Give the extent of all Plasmodium falciparum-infected red blood cells.
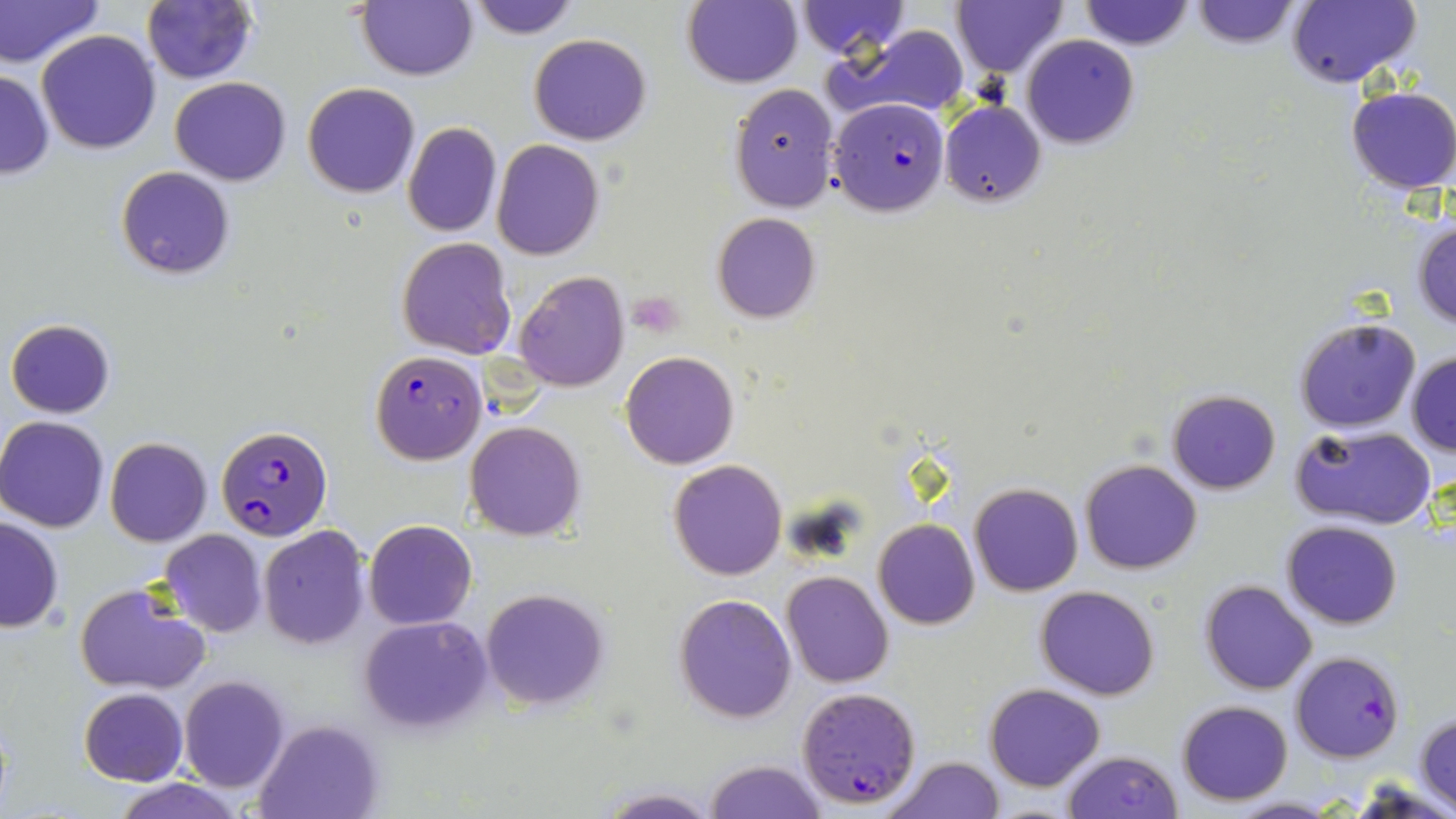
Approximate bounding boxes as (x1,y1)-(x2,y2) corner pairs in pixels.
Plasmodium falciparum-infected red blood cells: (829,97)-(950,216), (370,351)-(486,464), (217,424)-(332,541), (1291,650)-(1404,762), (797,686)-(923,810).

Summary:
  - Uninfected red blood cell locations: (0,0)-(104,69), (356,0)-(476,81), (465,0)-(579,39), (796,0)-(909,58), (951,0)-(1068,78), (1078,0)-(1196,52), (1289,0)-(1421,87), (140,1)-(258,85), (681,1)-(802,88), (1187,1)-(1303,51), (836,24)-(972,122), (37,31)-(161,154), (528,33)-(653,146), (1021,35)-(1139,148), (0,69)-(53,179), (169,77)-(292,185), (301,82)-(421,199), (729,83)-(840,213), (1345,86)-(1456,194), (939,101)-(1046,206), (401,122)-(501,237), (493,138)-(603,259), (115,165)-(235,279), (713,211)-(821,323), (1411,219)-(1456,330), (395,238)-(517,359), (513,272)-(629,392), (1294,317)-(1422,434), (5,318)-(115,418), (1406,350)-(1456,457), (621,351)-(739,469), (1166,388)-(1283,494), (0,416)-(111,532), (463,420)-(586,541), (1291,425)-(1439,531), (105,437)-(212,546), (669,457)-(788,580), (1080,459)-(1201,573), (969,483)-(1082,597), (0,516)-(65,633), (363,519)-(477,631), (874,519)-(980,630), (1281,520)-(1403,629), (257,526)-(370,649), (159,529)-(267,638), (780,570)-(893,686), (1200,580)-(1318,695), (74,581)-(211,695), (1036,585)-(1159,699), (480,588)-(609,711), (674,594)-(797,723), (359,617)-(493,735), (178,675)-(290,793), (984,682)-(1103,791), (78,689)-(186,786), (1176,700)-(1293,805), (1415,710)-(1456,813), (255,719)-(382,818), (1061,749)-(1183,818), (883,756)-(1004,819), (704,759)-(827,819), (111,777)-(243,819), (597,788)-(718,819), (1226,798)-(1343,819)
  - Platelet locations: (626,291)-(686,338)
  - Slide-level diagnosis: Plasmodium falciparum
  - Field of view: single
  - Stain: May-Grünwald-Giemsa
  - Image size: 1456×819 pixels
  - Preparation: thin blood film
  - Modality: optical microscopy
  - Magnification: 1000x